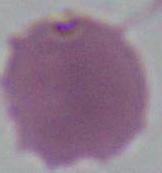
identification = erythrocyte
modality = micrograph
magnification = 1000x